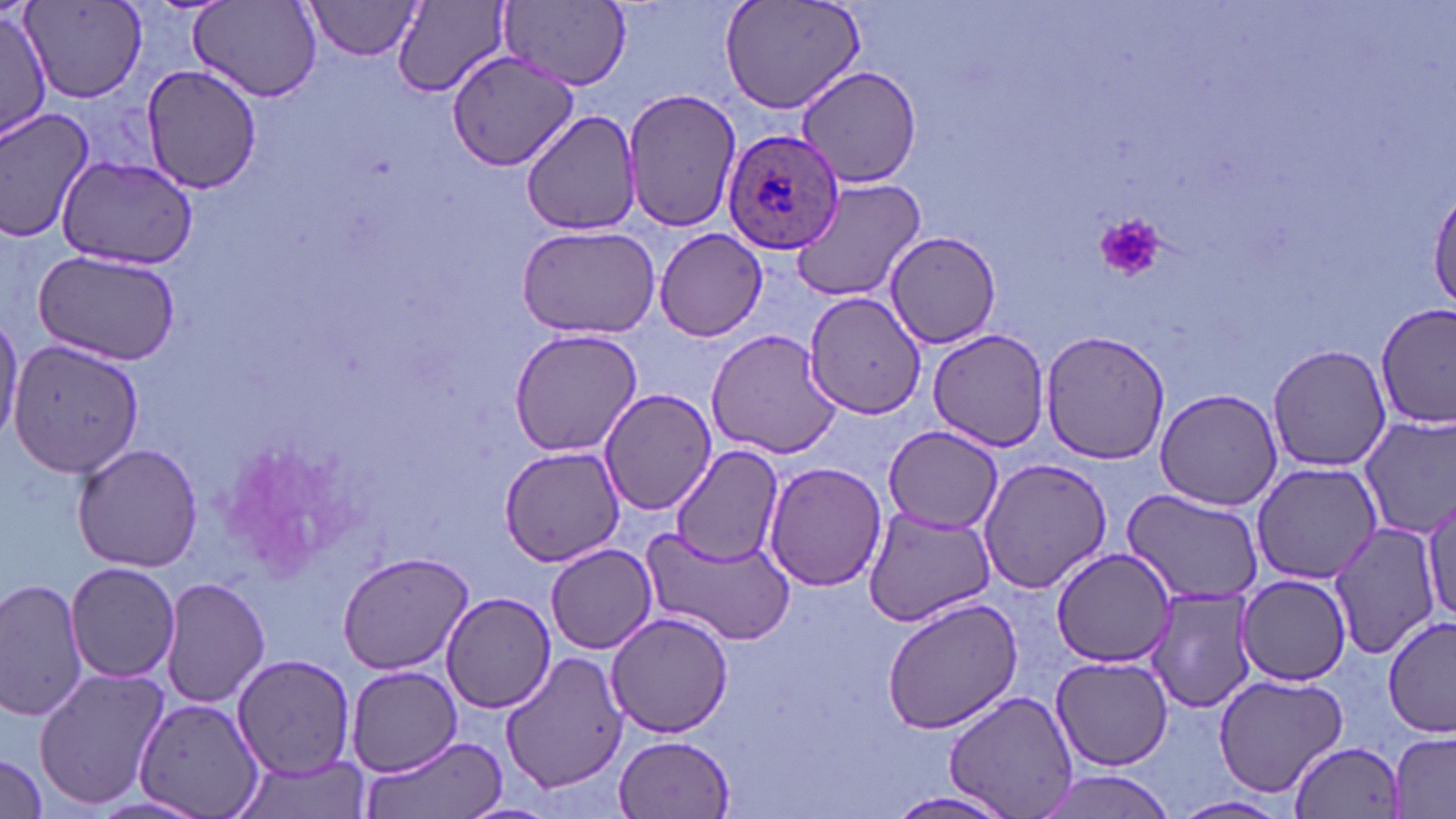

slide-level diagnosis = Plasmodium ovale
modality = optical microscopy
stain = May-Grünwald-Giemsa
field of view = single
uninfected red blood cell locations = approximate bounding boxes as (x1,y1)-(x2,y2) corner pairs in pixels: (20,0)-(146,102), (721,0)-(866,119), (190,1)-(324,104), (305,1)-(428,60), (395,1)-(513,96), (502,2)-(631,89), (0,5)-(52,143), (445,50)-(578,174), (139,63)-(263,194), (796,64)-(924,189), (621,87)-(741,235), (0,104)-(96,244), (521,109)-(643,237), (58,156)-(198,270), (792,176)-(927,303), (1430,188)-(1456,311), (515,223)-(660,338), (653,227)-(770,342), (884,231)-(1002,349), (30,247)-(183,365), (803,290)-(927,419), (1377,306)-(1453,428), (0,309)-(22,448), (507,327)-(642,457), (927,328)-(1051,451), (704,329)-(843,460), (1041,330)-(1170,466), (9,338)-(144,478), (1267,345)-(1391,472), (599,387)-(718,516), (1155,387)-(1282,511), (1355,413)-(1456,540), (882,424)-(1004,532), (72,442)-(203,572), (670,444)-(784,566), (499,445)-(627,568), (976,455)-(1114,597), (1251,461)-(1384,585), (764,462)-(887,591), (1422,490)-(1454,633), (1123,491)-(1262,604), (863,504)-(999,626), (1324,520)-(1443,659), (641,526)-(796,646), (547,543)-(659,653), (1052,549)-(1177,671), (337,551)-(473,675), (66,562)-(180,683), (161,575)-(269,708), (1237,575)-(1353,686), (0,577)-(90,723), (1145,587)-(1257,714), (440,592)-(556,713), (883,597)-(1024,735), (606,611)-(732,738), (1382,615)-(1456,736), (502,650)-(628,794), (1051,654)-(1173,770), (233,655)-(357,777), (347,666)-(461,775), (33,667)-(169,812), (1214,675)-(1348,794), (944,691)-(1080,819), (138,696)-(264,819), (1389,732)-(1454,819), (615,733)-(735,817), (362,737)-(508,819), (1288,738)-(1407,819), (0,754)-(47,818), (228,755)-(373,819), (1029,770)-(1180,818), (884,789)-(1021,819), (1170,795)-(1291,819)
Plasmodium ovale-infected red blood cell locations = approximate bounding boxes as (x1,y1)-(x2,y2) corner pairs in pixels: (723,128)-(845,253)
magnification = 1000x
image size = 1456×819 pixels
platelet locations = approximate bounding boxes as (x1,y1)-(x2,y2) corner pairs in pixels: (1094,215)-(1167,280)
preparation = thin blood film